Classify this cell by malaria status.
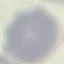
It is uninfected.

Summary:
  - Stain: Giemsa
  - Capture: smartphone camera at the microscope eyepiece
  - Image type: automatically extracted cell patch, resized to 64 × 64 pixels
  - Preparation: thin smear